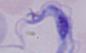

Photomicrograph. A trypanosome is shown. 1000x magnification.